Comment on the morphology of the erythrocytes.
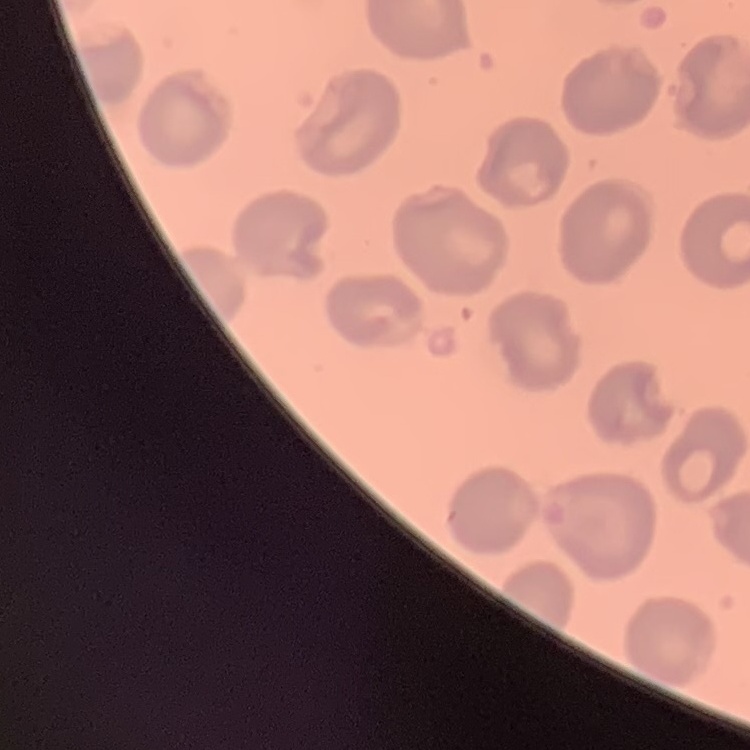

They show no rouleaux formation.

Stained with either Field's or Giemsa. Thin blood smear. Square crop of a larger photomicrograph.